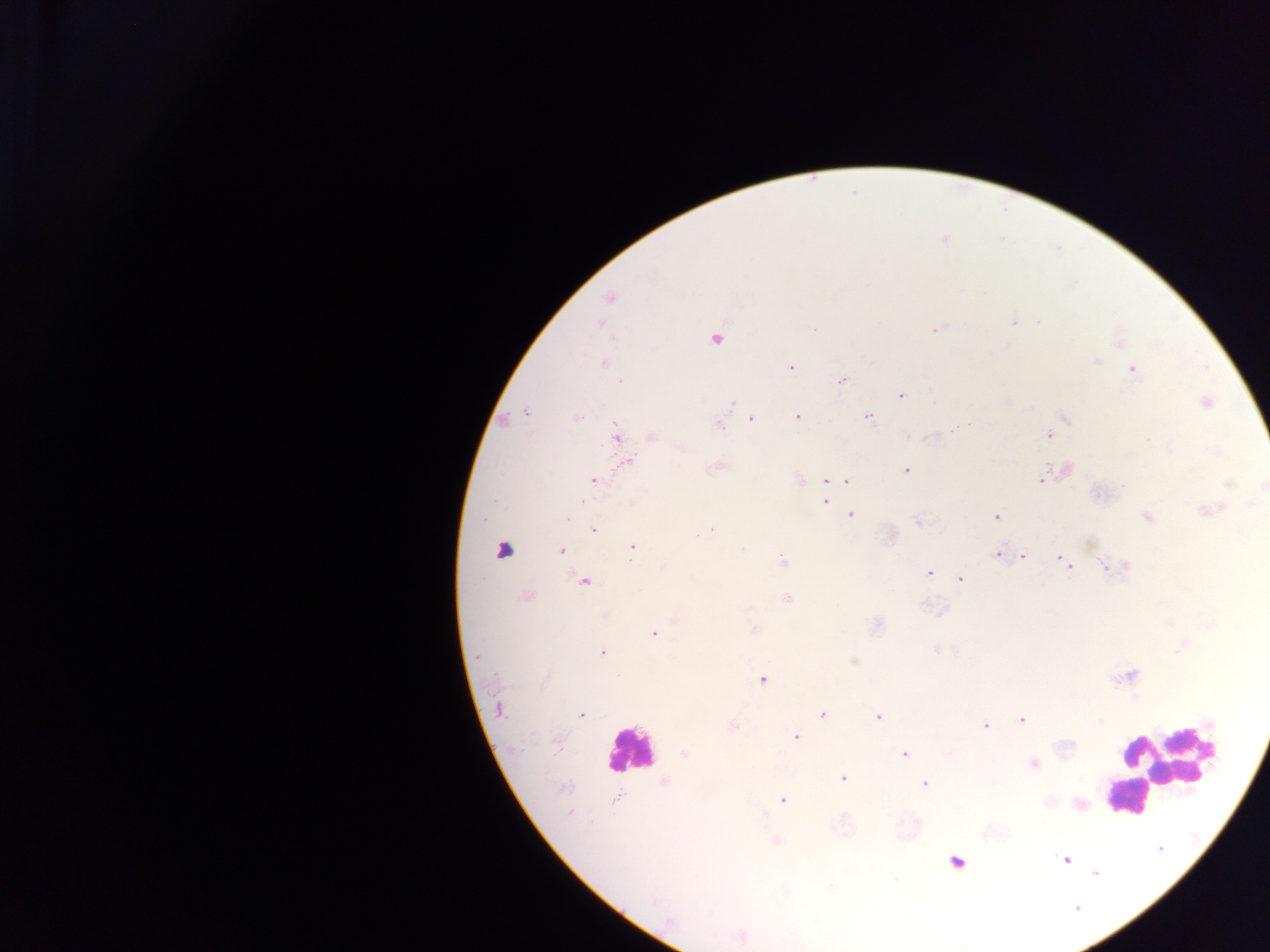

Approximate centers as x y in pixels. Plasmodium parasite locations: 609 298; 1012 321; 599 323; 937 328; 716 337; 1121 344; 1096 361; 603 363; 790 367; 1131 369; 842 380; 901 394; 1204 401; 526 412; 797 415; 751 417; 868 417; 1064 417; 575 418; 718 423; 1049 435; 615 437; 651 437; 627 461; 714 467; 1065 469; 907 470; 592 479; 798 479; 1042 479; 827 480; 847 481; 824 500; 631 503; 1208 509; 851 514; 995 517; 566 518; 1147 518; 918 521; 593 530; 889 536; 632 547; 502 550; 560 551; 998 554; 1022 556; 1061 558; 784 562; 1068 565; 1124 565; 1107 566; 929 572; 959 578; 584 581; 527 595; 787 599; 605 616; 875 625; 753 629; 653 633; 602 652; 762 678; 498 709; 581 715; 823 715; 878 716; 1021 719; 985 725; 731 726; 795 736; 684 754; 905 754; 1033 763; 843 778; 664 782; 924 783; 781 799; 1078 804; 570 813; 777 842; 1066 860; 955 861; 741 936. Leukocyte locations: 629 750; 1164 764; 1136 796; 1128 797. Thick blood smear. Photographed through a microscope with a mobile-phone camera. Single field of view. Sample from Ghana. Image is 1270×952 pixels.